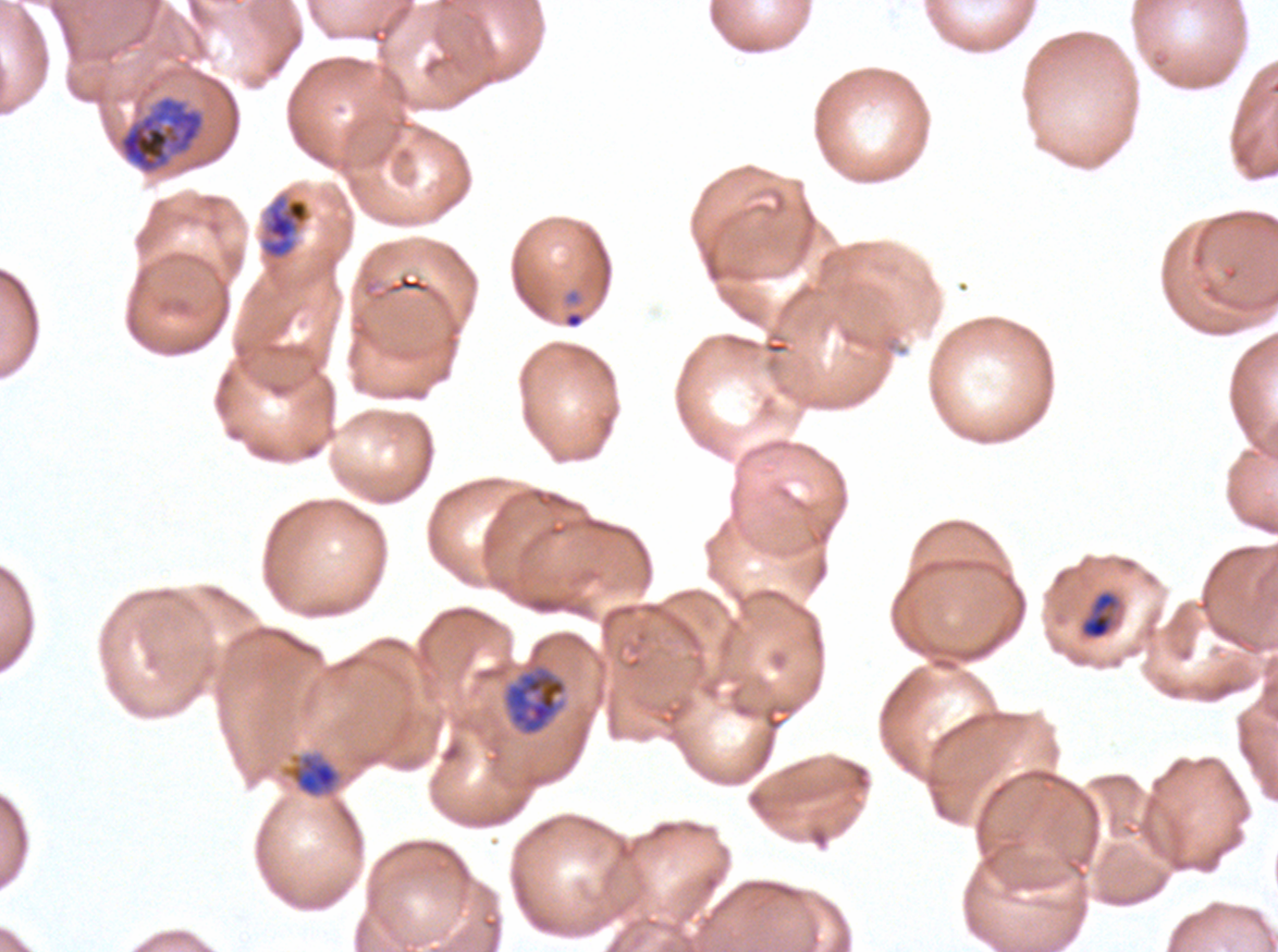

Approximate bounding boxes as {x1, y1, x2, y2} in pixels.
Summary:
  - Early schizont locations: {118, 96, 204, 174}
  - Mid trophozoite locations: {281, 751, 342, 799}
  - Late-ring/early-trophozoite locations: {1079, 590, 1121, 641}
  - Ring locations: {565, 312, 583, 328}
  - Late trophozoite locations: {263, 197, 310, 259}, {502, 665, 568, 736}
  - Specimen: ex-vivo Plasmodium falciparum culture from a patient in The Gambia, grown for 24 to 48 hours
  - Stain: Giemsa
  - Life-cycle stages observed: ring, late-ring/early-trophozoite, mid trophozoite, late trophozoite, early schizont
  - Preparation: thin blood film
  - Image size: 1278×952 pixels
  - Field of view: one sub-image of a larger composite